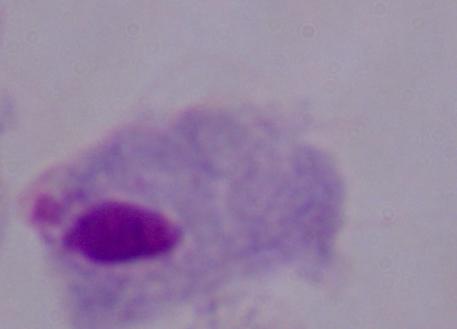
A trichomonad is shown. Micrograph. 1000x magnification.